Report the malaria status of this cell.
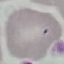
It is uninfected.

{
  "preparation": "thin blood film",
  "capture": "smartphone camera at the microscope eyepiece",
  "image_type": "cell patch, automatically extracted from a larger field of view and resized to 64 × 64 pixels",
  "stain": "Giemsa"
}